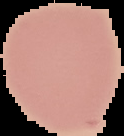

Image is 124×136 pixels. Malaria status: uninfected. The area outside the segmented cell region is set to black. From a thin blood film.